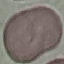
Summary:
  - Result: no malaria parasites seen
  - Stain: Giemsa
  - Image type: automatically extracted cell patch, resized to 64 × 64 pixels
  - Preparation: thin blood smear
  - Capture: smartphone camera at the microscope eyepiece